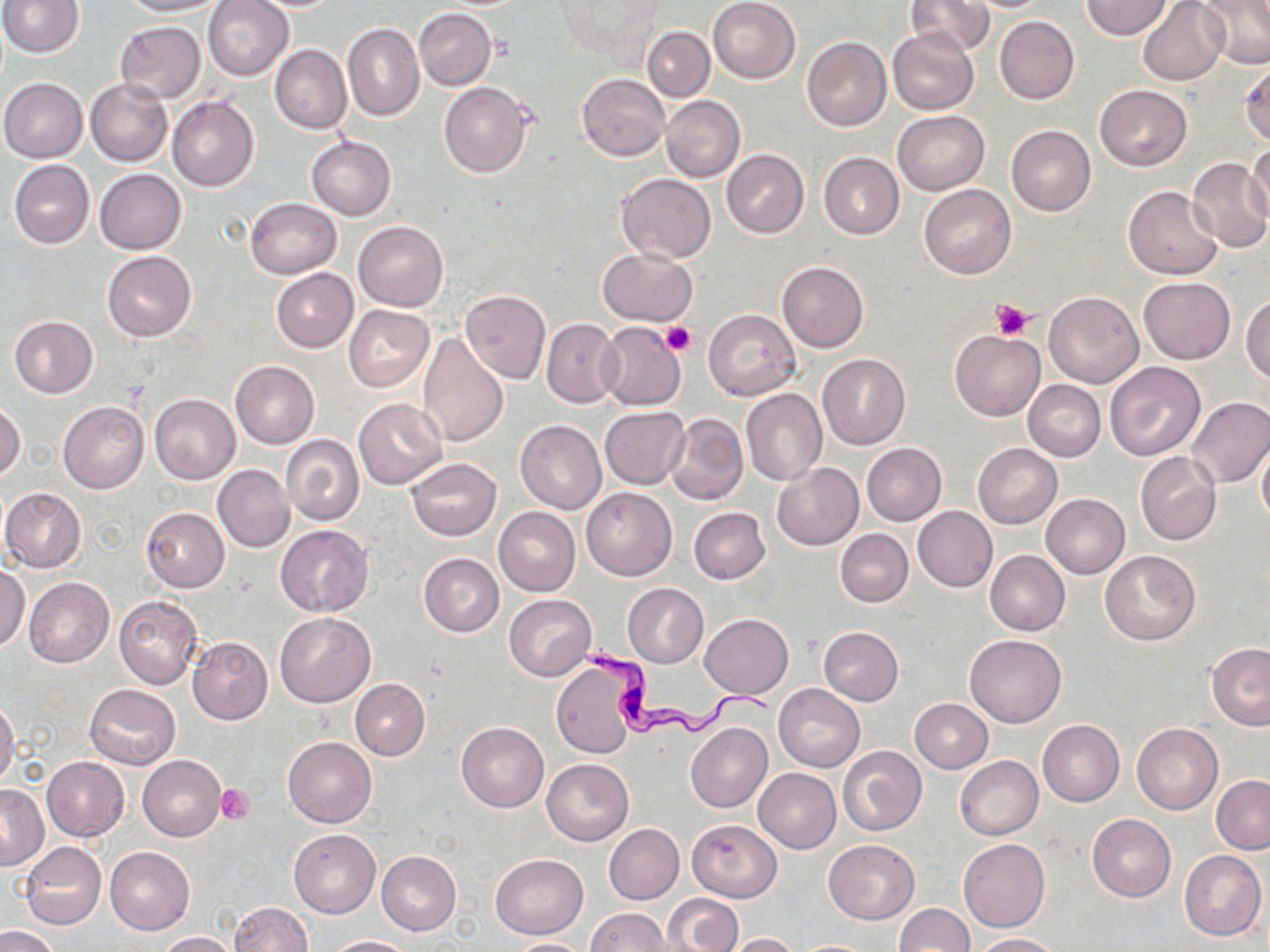 Approximate bounding boxes as named x1/y1/x2/y2 corners in pixels. Uninfected red blood cell locations: (x1=1, y1=0, x2=82, y2=56), (x1=118, y1=0, x2=222, y2=17), (x1=203, y1=0, x2=294, y2=80), (x1=708, y1=0, x2=801, y2=83), (x1=905, y1=0, x2=992, y2=57), (x1=1198, y1=0, x2=1270, y2=70), (x1=554, y1=1, x2=664, y2=64), (x1=956, y1=1, x2=1055, y2=12), (x1=1082, y1=1, x2=1171, y2=39), (x1=1137, y1=1, x2=1229, y2=85), (x1=413, y1=9, x2=495, y2=90), (x1=995, y1=16, x2=1079, y2=104), (x1=115, y1=20, x2=207, y2=102), (x1=344, y1=24, x2=423, y2=121), (x1=642, y1=26, x2=714, y2=101), (x1=888, y1=26, x2=978, y2=114), (x1=802, y1=38, x2=890, y2=131), (x1=270, y1=45, x2=351, y2=134), (x1=1240, y1=57, x2=1270, y2=147), (x1=577, y1=73, x2=669, y2=161), (x1=0, y1=78, x2=87, y2=162), (x1=86, y1=79, x2=172, y2=167), (x1=439, y1=82, x2=532, y2=178), (x1=1094, y1=85, x2=1192, y2=170), (x1=167, y1=96, x2=259, y2=192), (x1=660, y1=96, x2=745, y2=183), (x1=894, y1=111, x2=988, y2=195), (x1=1007, y1=125, x2=1095, y2=215), (x1=307, y1=138, x2=396, y2=220), (x1=1246, y1=144, x2=1270, y2=225), (x1=722, y1=150, x2=808, y2=238), (x1=819, y1=152, x2=904, y2=239), (x1=1185, y1=156, x2=1270, y2=252), (x1=10, y1=159, x2=94, y2=248), (x1=95, y1=169, x2=186, y2=254), (x1=616, y1=173, x2=716, y2=263), (x1=919, y1=184, x2=1016, y2=278), (x1=1123, y1=187, x2=1222, y2=279), (x1=244, y1=198, x2=341, y2=278), (x1=354, y1=221, x2=447, y2=310), (x1=598, y1=248, x2=697, y2=325), (x1=103, y1=251, x2=196, y2=342), (x1=777, y1=262, x2=868, y2=352), (x1=271, y1=268, x2=358, y2=353), (x1=1139, y1=277, x2=1235, y2=364), (x1=459, y1=289, x2=549, y2=384), (x1=1043, y1=292, x2=1144, y2=387), (x1=1243, y1=296, x2=1270, y2=385), (x1=344, y1=305, x2=433, y2=390), (x1=704, y1=309, x2=800, y2=400), (x1=8, y1=316, x2=98, y2=398), (x1=542, y1=318, x2=621, y2=407), (x1=597, y1=321, x2=686, y2=410), (x1=417, y1=331, x2=510, y2=448), (x1=949, y1=331, x2=1044, y2=421), (x1=818, y1=355, x2=909, y2=448), (x1=230, y1=361, x2=319, y2=448), (x1=1105, y1=362, x2=1205, y2=460), (x1=1024, y1=380, x2=1106, y2=461), (x1=742, y1=389, x2=827, y2=486), (x1=150, y1=394, x2=240, y2=484), (x1=1186, y1=397, x2=1270, y2=489), (x1=353, y1=399, x2=446, y2=489), (x1=58, y1=401, x2=149, y2=494), (x1=0, y1=402, x2=25, y2=480), (x1=599, y1=406, x2=690, y2=488), (x1=665, y1=412, x2=749, y2=506), (x1=515, y1=420, x2=606, y2=513), (x1=281, y1=435, x2=365, y2=527), (x1=1257, y1=441, x2=1270, y2=528), (x1=862, y1=443, x2=946, y2=525), (x1=974, y1=443, x2=1062, y2=528), (x1=1135, y1=452, x2=1221, y2=544), (x1=406, y1=457, x2=501, y2=540), (x1=771, y1=463, x2=864, y2=550), (x1=213, y1=465, x2=294, y2=552), (x1=2, y1=487, x2=86, y2=573), (x1=581, y1=488, x2=677, y2=580), (x1=1041, y1=494, x2=1129, y2=578), (x1=913, y1=506, x2=998, y2=592), (x1=142, y1=507, x2=229, y2=592), (x1=494, y1=507, x2=580, y2=596), (x1=688, y1=508, x2=770, y2=584), (x1=275, y1=525, x2=372, y2=616), (x1=836, y1=529, x2=912, y2=607), (x1=1099, y1=549, x2=1200, y2=644), (x1=985, y1=550, x2=1070, y2=635), (x1=419, y1=553, x2=504, y2=636), (x1=0, y1=565, x2=30, y2=653), (x1=24, y1=578, x2=113, y2=667), (x1=623, y1=583, x2=708, y2=667), (x1=114, y1=595, x2=205, y2=690), (x1=504, y1=595, x2=596, y2=681), (x1=274, y1=613, x2=374, y2=706), (x1=699, y1=613, x2=793, y2=698), (x1=819, y1=626, x2=903, y2=705), (x1=964, y1=634, x2=1065, y2=727), (x1=187, y1=637, x2=272, y2=725), (x1=1207, y1=643, x2=1270, y2=730), (x1=551, y1=656, x2=644, y2=758), (x1=351, y1=678, x2=430, y2=760), (x1=85, y1=684, x2=180, y2=769), (x1=773, y1=684, x2=864, y2=771), (x1=910, y1=698, x2=992, y2=773), (x1=0, y1=699, x2=20, y2=790), (x1=1038, y1=720, x2=1123, y2=807), (x1=457, y1=722, x2=549, y2=812), (x1=686, y1=723, x2=771, y2=812), (x1=1132, y1=723, x2=1223, y2=814), (x1=283, y1=737, x2=376, y2=827), (x1=837, y1=745, x2=926, y2=836), (x1=40, y1=752, x2=121, y2=926), (x1=137, y1=755, x2=226, y2=841), (x1=954, y1=756, x2=1044, y2=840), (x1=42, y1=757, x2=130, y2=841), (x1=542, y1=758, x2=634, y2=846), (x1=754, y1=768, x2=841, y2=852), (x1=1212, y1=776, x2=1270, y2=854), (x1=1, y1=786, x2=48, y2=869), (x1=1087, y1=813, x2=1175, y2=901), (x1=687, y1=819, x2=781, y2=902), (x1=604, y1=823, x2=684, y2=904), (x1=289, y1=830, x2=380, y2=917), (x1=958, y1=838, x2=1049, y2=932), (x1=822, y1=840, x2=918, y2=924), (x1=20, y1=842, x2=107, y2=929), (x1=106, y1=846, x2=195, y2=935), (x1=1179, y1=850, x2=1267, y2=942), (x1=376, y1=851, x2=461, y2=935), (x1=490, y1=853, x2=588, y2=938), (x1=661, y1=893, x2=741, y2=952), (x1=229, y1=902, x2=313, y2=952), (x1=893, y1=903, x2=973, y2=952), (x1=584, y1=908, x2=671, y2=951), (x1=0, y1=926, x2=62, y2=952), (x1=156, y1=932, x2=238, y2=952), (x1=726, y1=933, x2=801, y2=952), (x1=974, y1=933, x2=1058, y2=952), (x1=324, y1=936, x2=421, y2=952), (x1=502, y1=938, x2=594, y2=951), (x1=792, y1=939, x2=881, y2=951). Platelet locations: (x1=991, y1=298, x2=1034, y2=339), (x1=661, y1=321, x2=697, y2=356), (x1=215, y1=785, x2=254, y2=824). Trypanosoma brucei locations: (x1=580, y1=643, x2=781, y2=737). Slide-level diagnosis: Trypanosoma brucei. Single field of view. Image is 1270×952 pixels. Captured at 1000x magnification. Optical microscopy. May-Grünwald-Giemsa-stained preparation. Thin blood film.